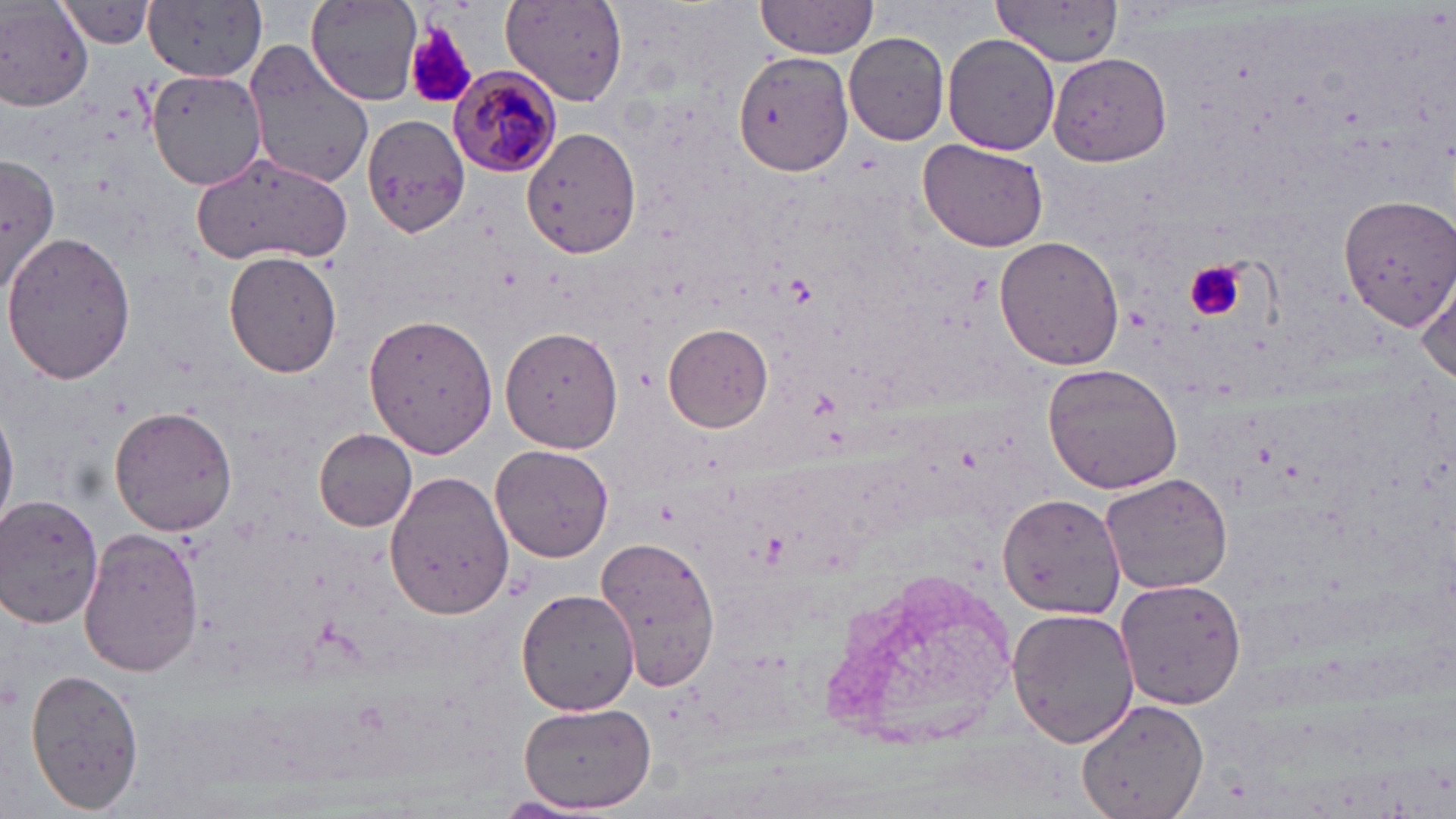
Summary:
  - Coordinate format: approximate bounding boxes as named x1/y1/x2/y2 corners in pixels
  - Plasmodium malariae-infected red blood cell locations: (x1=448, y1=68, x2=560, y2=177)
  - Uninfected red blood cell locations: (x1=144, y1=0, x2=269, y2=82), (x1=305, y1=0, x2=424, y2=105), (x1=501, y1=1, x2=630, y2=106), (x1=756, y1=1, x2=880, y2=57), (x1=995, y1=2, x2=1125, y2=69), (x1=0, y1=3, x2=95, y2=109), (x1=52, y1=3, x2=157, y2=48), (x1=844, y1=33, x2=951, y2=146), (x1=943, y1=33, x2=1061, y2=155), (x1=242, y1=43, x2=376, y2=190), (x1=733, y1=51, x2=855, y2=176), (x1=1048, y1=51, x2=1172, y2=167), (x1=147, y1=67, x2=266, y2=192), (x1=363, y1=113, x2=471, y2=239), (x1=522, y1=126, x2=641, y2=259), (x1=917, y1=141, x2=1050, y2=254), (x1=192, y1=151, x2=354, y2=270), (x1=0, y1=154, x2=62, y2=295), (x1=1334, y1=190, x2=1454, y2=333), (x1=1336, y1=191, x2=1456, y2=329), (x1=1, y1=233, x2=133, y2=385), (x1=995, y1=237, x2=1125, y2=371), (x1=225, y1=250, x2=342, y2=377), (x1=1414, y1=273, x2=1456, y2=385), (x1=363, y1=311, x2=498, y2=459), (x1=664, y1=322, x2=774, y2=433), (x1=500, y1=324, x2=624, y2=454), (x1=1043, y1=361, x2=1184, y2=495), (x1=0, y1=402, x2=17, y2=533), (x1=110, y1=406, x2=236, y2=535), (x1=314, y1=429, x2=418, y2=531), (x1=490, y1=445, x2=615, y2=562), (x1=383, y1=470, x2=515, y2=620), (x1=1099, y1=471, x2=1233, y2=595), (x1=997, y1=491, x2=1126, y2=618), (x1=0, y1=492, x2=104, y2=626), (x1=79, y1=527, x2=203, y2=678), (x1=595, y1=533, x2=723, y2=694), (x1=816, y1=565, x2=1024, y2=751), (x1=1115, y1=576, x2=1247, y2=711), (x1=516, y1=589, x2=639, y2=716), (x1=1007, y1=606, x2=1138, y2=749), (x1=26, y1=666, x2=145, y2=812), (x1=1076, y1=698, x2=1209, y2=819), (x1=518, y1=703, x2=656, y2=814), (x1=493, y1=795, x2=607, y2=819)
  - Platelet locations: (x1=399, y1=20, x2=480, y2=111), (x1=1185, y1=260, x2=1245, y2=322)
  - Slide-level diagnosis: Plasmodium malariae
  - Field of view: one of a larger specimen
  - Preparation: thin blood film
  - Modality: light microscopy
  - Image size: 1456×819 pixels
  - Stain: May-Grünwald-Giemsa
  - Magnification: 1000x